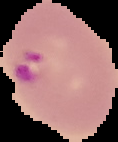

Result: malaria parasites detected. From a thin blood smear. Image is 118×142 pixels. The area outside the segmented cell region is set to black.